Classify this cell by malaria status.
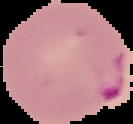

It is parasitized.

Summary:
  - Image type: segmented cell region with the area outside set to black
  - Preparation: thin blood smear
  - Image size: 133×124 pixels